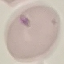
Summary:
  - Malaria status: uninfected
  - Stain: Giemsa
  - Capture: smartphone camera at the microscope eyepiece
  - Image type: cell patch, automatically extracted from a larger field of view and resized to 64 × 64 pixels
  - Preparation: thin smear